Name the blood parasite species.
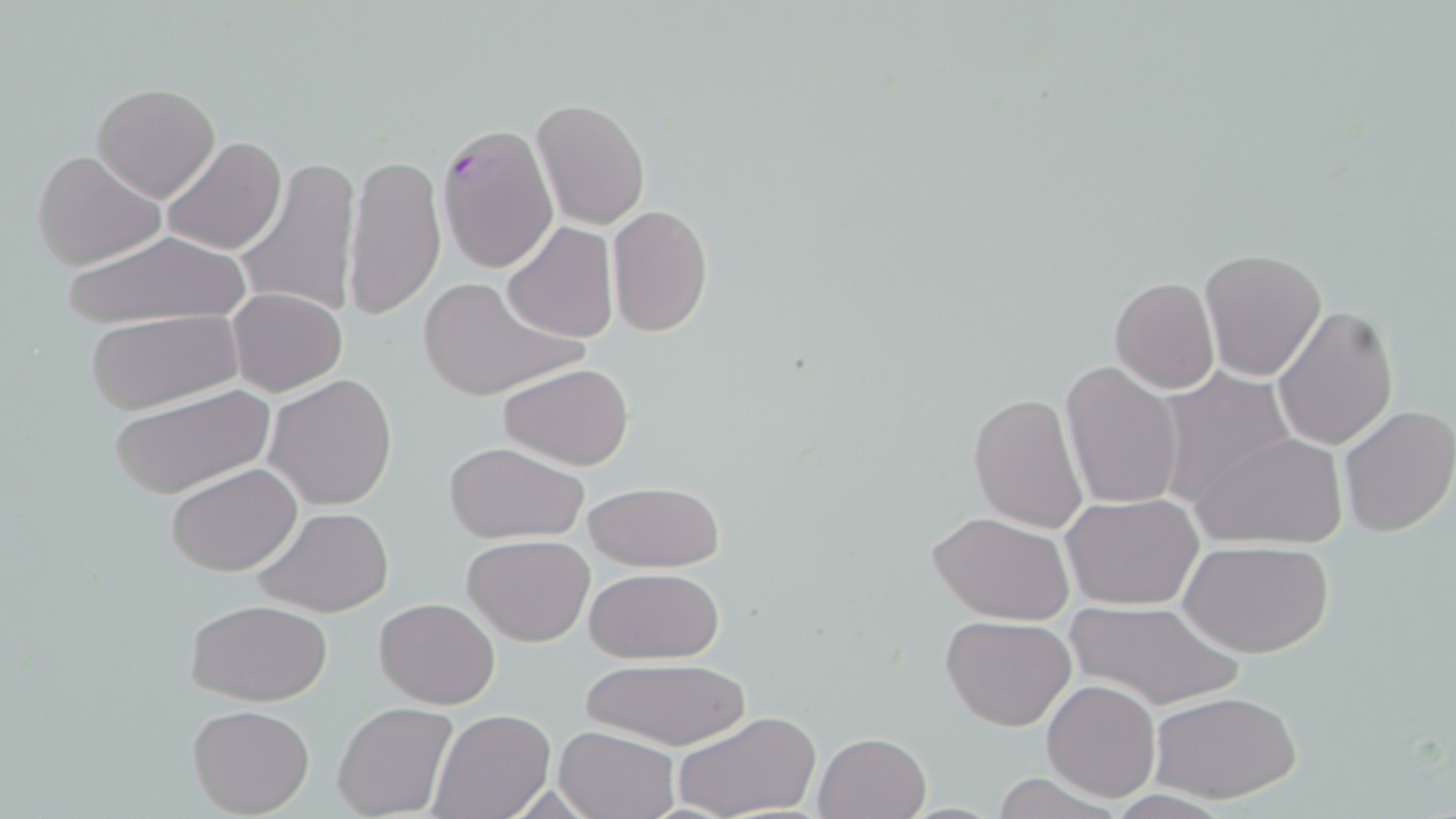

Plasmodium falciparum.

uninfected red blood cell locations = approximate bounding boxes as (x1,y1)-(x2,y2) corner pairs in pixels: (91,82)-(221,201), (532,99)-(650,229), (161,135)-(288,256), (31,148)-(167,271), (343,150)-(447,322), (237,155)-(360,318), (606,204)-(714,337), (501,222)-(618,342), (58,229)-(252,330), (1198,249)-(1325,380), (416,274)-(586,404), (1109,276)-(1220,394), (228,289)-(347,395), (1273,305)-(1400,451), (85,311)-(242,415), (1061,360)-(1184,512), (498,361)-(635,470), (1157,370)-(1298,513), (264,373)-(398,510), (106,384)-(279,499), (968,391)-(1089,533), (1337,405)-(1456,538), (1192,430)-(1349,549), (442,441)-(590,545), (168,462)-(303,576), (582,479)-(724,573), (1062,492)-(1204,610), (252,507)-(394,617), (928,510)-(1074,623), (462,534)-(594,646), (1182,541)-(1332,659), (583,566)-(724,664), (375,596)-(499,709), (185,599)-(333,705), (1064,602)-(1239,712), (941,613)-(1077,730), (579,657)-(750,748), (1043,680)-(1160,801), (1152,691)-(1300,803), (333,701)-(458,819), (187,702)-(315,817), (430,709)-(554,819), (671,710)-(819,819), (554,727)-(680,819), (814,732)-(930,819)
Plasmodium falciparum-infected red blood cell locations = approximate bounding boxes as (x1,y1)-(x2,y2) corner pairs in pixels: (435,124)-(558,273)
stain = May-Grünwald-Giemsa
image size = 1456×819 pixels
field of view = one of a larger specimen
preparation = thin blood smear
modality = light microscopy
magnification = 1000x